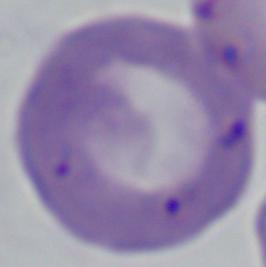 Micrograph. A Babesia parasite is shown. Captured at 1000x magnification.